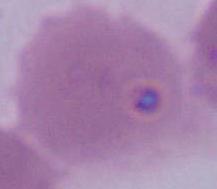 A red blood cell is shown. Captured at 1000x magnification. Micrograph.